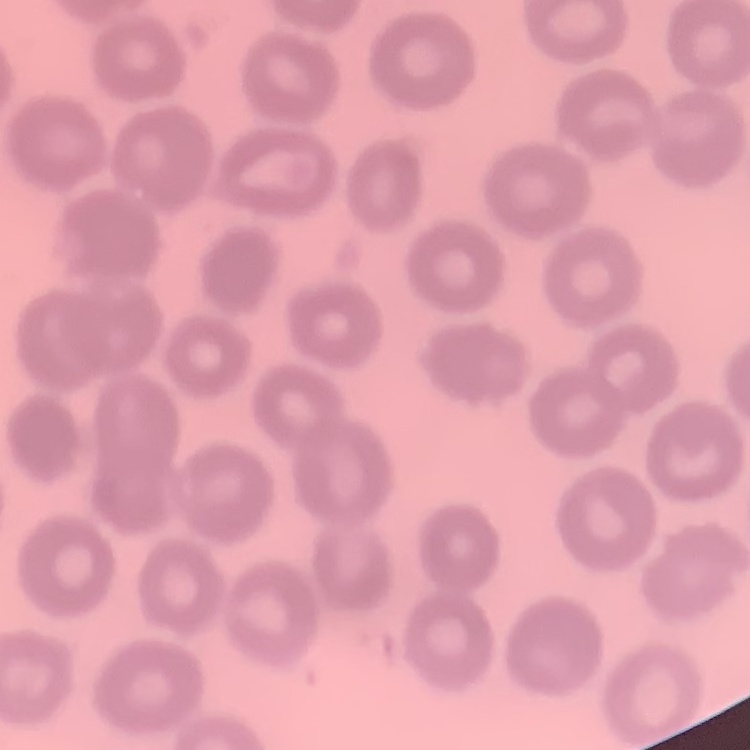

Summary:
  - Red blood cell morphology: no rouleaux formation
  - Image type: one tile cut from a larger photomicrograph
  - Preparation: thin blood film
  - Stain: Field's or Giemsa